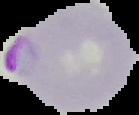
image_type: cell region segmented out of the field of view; surrounding area masked to black
image_size: 139×115 pixels
preparation: thin blood film
result: malaria parasites detected